Classify the preparation.
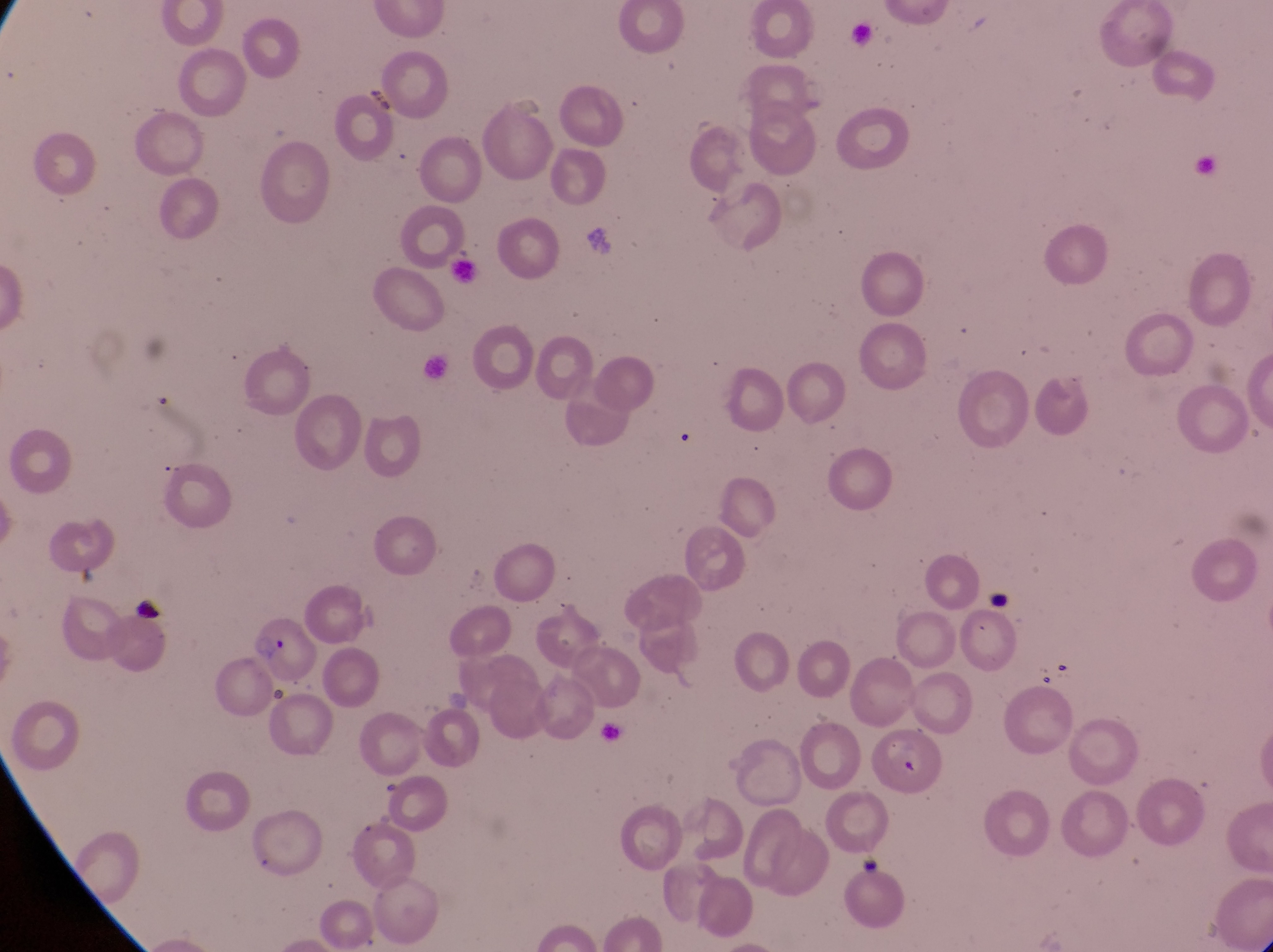
This is a thin smear.

artifact (platelet-like body, stain precipitate, or debris) locations = approximate bounding boxes as {left, top, right, bottom} in pixels: {988, 587, 1012, 621}, {131, 598, 163, 627}, {855, 849, 883, 877}
image size = 1273×952 pixels
field of view = single
magnification = 1000x
parasitised red blood cell locations = approximate bounding boxes as {left, top, right, bottom} in pixels: {250, 621, 319, 688}
capture = smartphone photograph through the eyepiece of an Olympus CX-23 microscope
country = Uganda